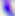
identification = Toxoplasma gondii
modality = photomicrograph
magnification = 400x